Report the malaria status of this cell.
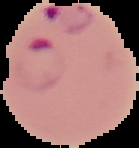

It is parasitized.

Summary:
  - Preparation: thin blood film
  - Image size: 139×148 pixels
  - Image type: cell region segmented out of the field of view; surrounding area masked to black